State which cell type is depicted.
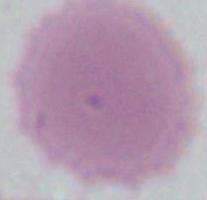
An erythrocyte.

magnification = 1000x
modality = photomicrograph